Identify the cell.
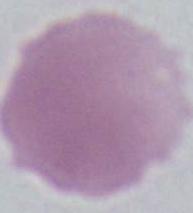

This is an erythrocyte.

magnification = 1000x
modality = micrograph